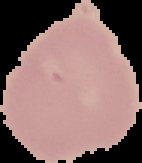

image_type: cell region segmented out of the field of view; surrounding area masked to black
preparation: thin blood smear
image_size: 142×163 pixels
malaria_status: uninfected